Identify the parasite.
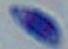

Toxoplasma gondii.

magnification: 1000x
modality: photomicrograph